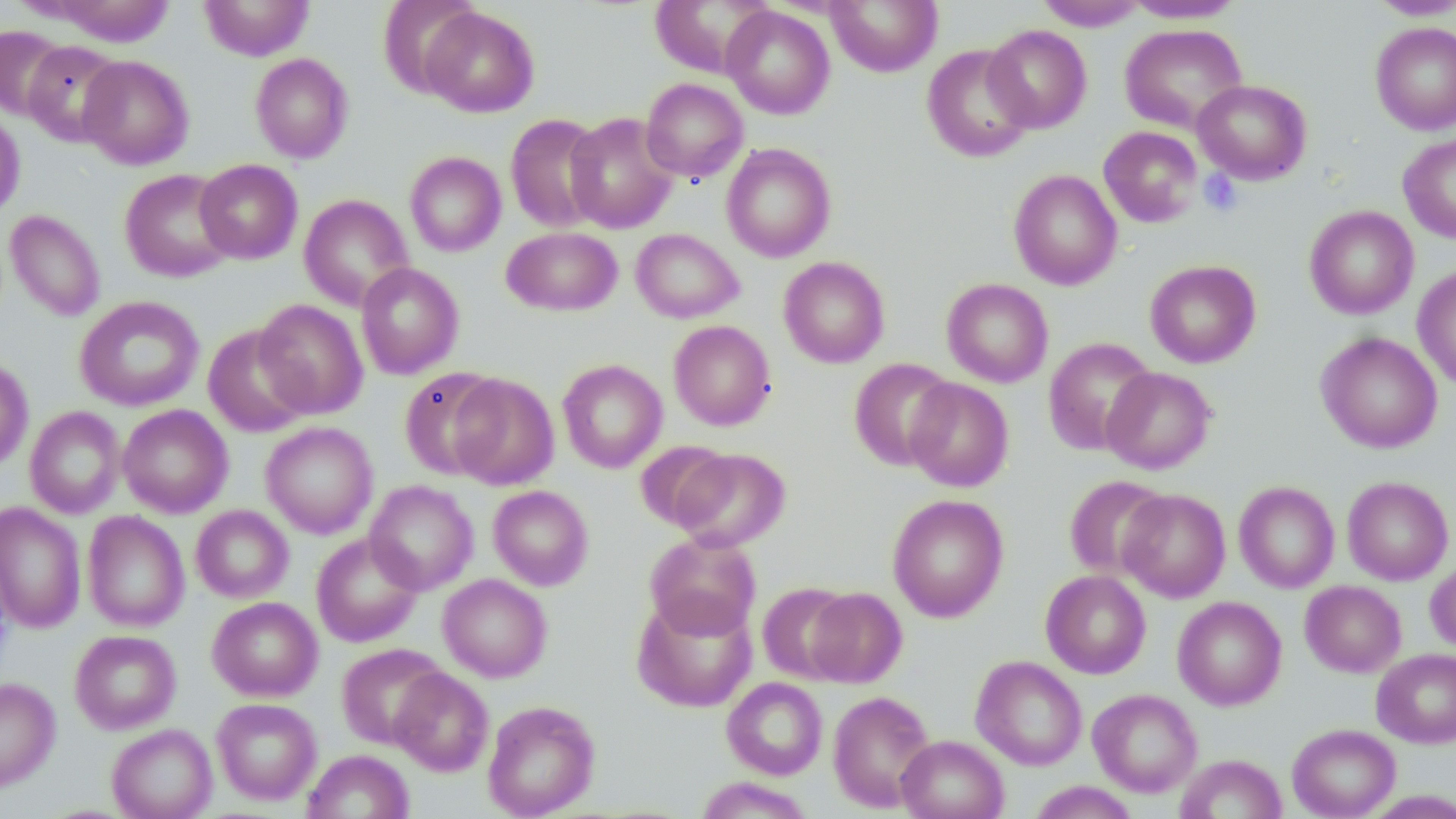
Summary:
  - Coordinate format: approximate bounding boxes as [x1, y1, x2, y2] in pixels
  - Uninfected red blood cell locations: [199, 0, 314, 61], [377, 0, 482, 98], [650, 0, 775, 77], [825, 0, 943, 77], [1366, 0, 1456, 20], [48, 1, 177, 47], [1035, 1, 1148, 30], [1119, 1, 1246, 23], [721, 5, 835, 119], [421, 6, 539, 117], [1370, 22, 1456, 135], [1119, 23, 1248, 133], [983, 24, 1092, 133], [0, 26, 70, 119], [22, 41, 125, 146], [921, 44, 1036, 163], [250, 53, 354, 163], [78, 55, 194, 170], [640, 78, 748, 182], [1193, 79, 1312, 184], [0, 110, 26, 221], [564, 112, 679, 233], [505, 114, 608, 232], [1098, 126, 1203, 228], [1398, 134, 1456, 243], [721, 143, 836, 262], [404, 151, 506, 256], [194, 159, 303, 264], [119, 168, 237, 282], [1008, 169, 1122, 290], [299, 194, 414, 311], [1304, 205, 1419, 319], [5, 210, 105, 321], [501, 226, 623, 316], [631, 228, 743, 323], [778, 256, 890, 368], [1144, 259, 1261, 368], [355, 262, 465, 379], [1412, 264, 1456, 391], [942, 278, 1054, 387], [74, 295, 205, 411], [254, 298, 368, 419], [669, 320, 776, 430], [202, 324, 312, 438], [1316, 331, 1443, 454], [1042, 337, 1157, 456], [0, 356, 34, 471], [848, 358, 957, 471], [557, 359, 668, 473], [399, 366, 506, 480], [1102, 367, 1216, 473], [448, 373, 559, 490], [905, 377, 1014, 492], [118, 405, 233, 517], [25, 406, 126, 518], [260, 421, 379, 538], [635, 441, 735, 532], [671, 448, 790, 551], [1063, 475, 1171, 580], [1342, 476, 1454, 585], [364, 480, 478, 595], [1234, 481, 1340, 593], [488, 485, 594, 590], [1117, 489, 1231, 602], [887, 494, 1009, 623], [0, 502, 86, 634], [191, 505, 293, 603], [82, 511, 190, 632], [644, 531, 762, 640], [311, 532, 423, 647], [1426, 559, 1456, 654], [1040, 570, 1151, 678], [438, 573, 552, 682], [757, 581, 857, 683], [1300, 581, 1406, 677], [803, 587, 907, 688], [631, 593, 757, 712], [207, 596, 322, 701], [1172, 596, 1287, 710], [70, 629, 181, 734], [336, 643, 450, 749], [1372, 649, 1456, 748], [971, 655, 1087, 770], [390, 668, 493, 776], [0, 677, 60, 792], [721, 677, 828, 780], [1088, 689, 1202, 796], [827, 690, 936, 811], [211, 698, 322, 804], [483, 700, 600, 818], [1287, 723, 1401, 818], [106, 724, 217, 819], [896, 735, 1008, 819], [302, 749, 414, 819], [1175, 754, 1287, 819], [695, 776, 816, 818], [1027, 781, 1140, 818], [1361, 789, 1456, 818]
  - Platelet locations: [1199, 169, 1243, 216]
  - Slide-level diagnosis: negative for blood parasites
  - Magnification: 1000x
  - Preparation: thin blood film
  - Stain: May-Grünwald-Giemsa
  - Modality: light microscopy
  - Image size: 1456×819 pixels
  - Field of view: one of a larger specimen